Assess the background quality.
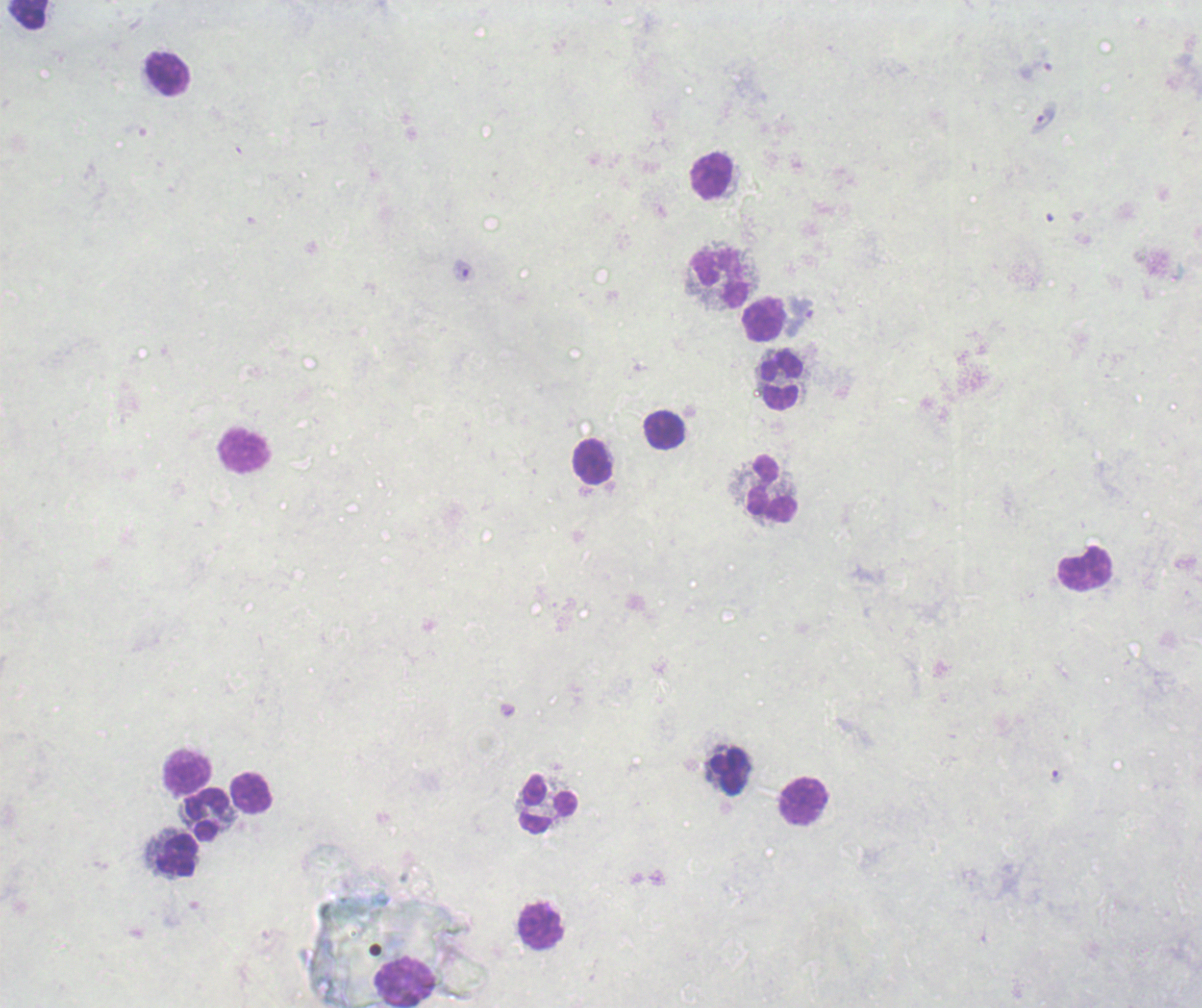
Poor.

Approximate centers as {x, y} in pixels.
Summary:
  - Trophozoite locations: {1042, 117}, {799, 317}, {1056, 776}
  - Leukocyte locations: {27, 14}, {168, 75}, {711, 175}, {721, 279}, {764, 320}, {780, 381}, {665, 430}, {245, 450}, {592, 462}, {771, 488}, {1084, 569}, {187, 771}, {730, 773}, {251, 793}, {803, 802}, {549, 805}, {206, 815}, {178, 856}, {540, 926}, {405, 984}
  - Context: previously used in a real diagnosis
  - Result: malaria parasites identified
  - Image size: 1202×1008 pixels
  - Magnification: 100x
  - Stain: Romanowsky
  - Preparation: thick blood film
  - Field of view: single